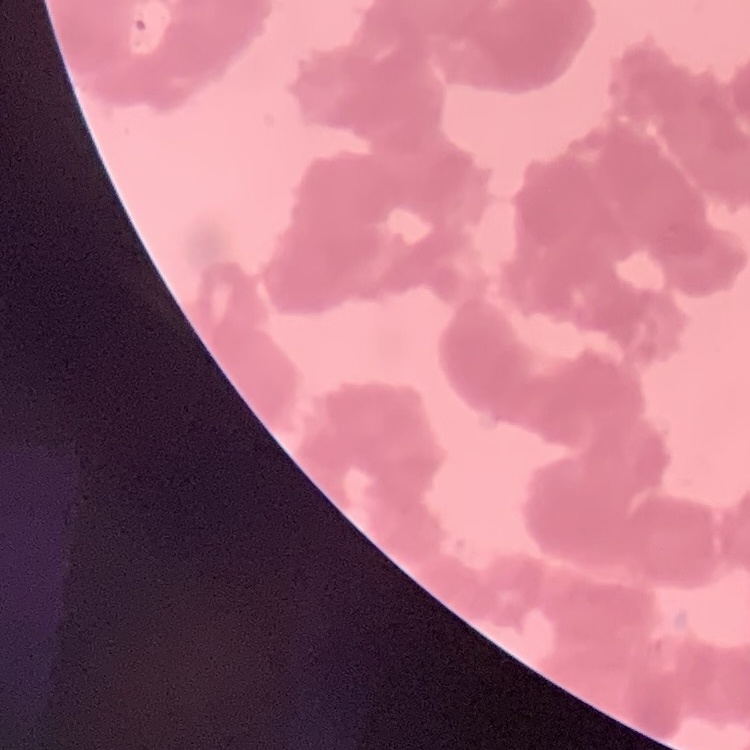
erythrocyte_morphology: rouleaux formation
preparation: thin blood smear
image_type: one tile cut from a larger photomicrograph
stain: Field's or Giemsa